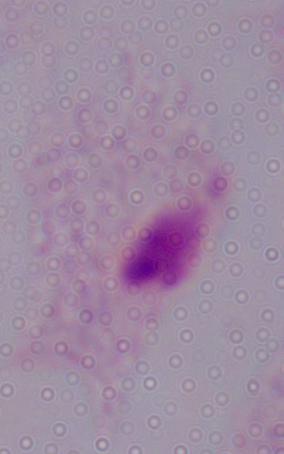
Captured at 1000x magnification. A trichomonad is seen. Micrograph.